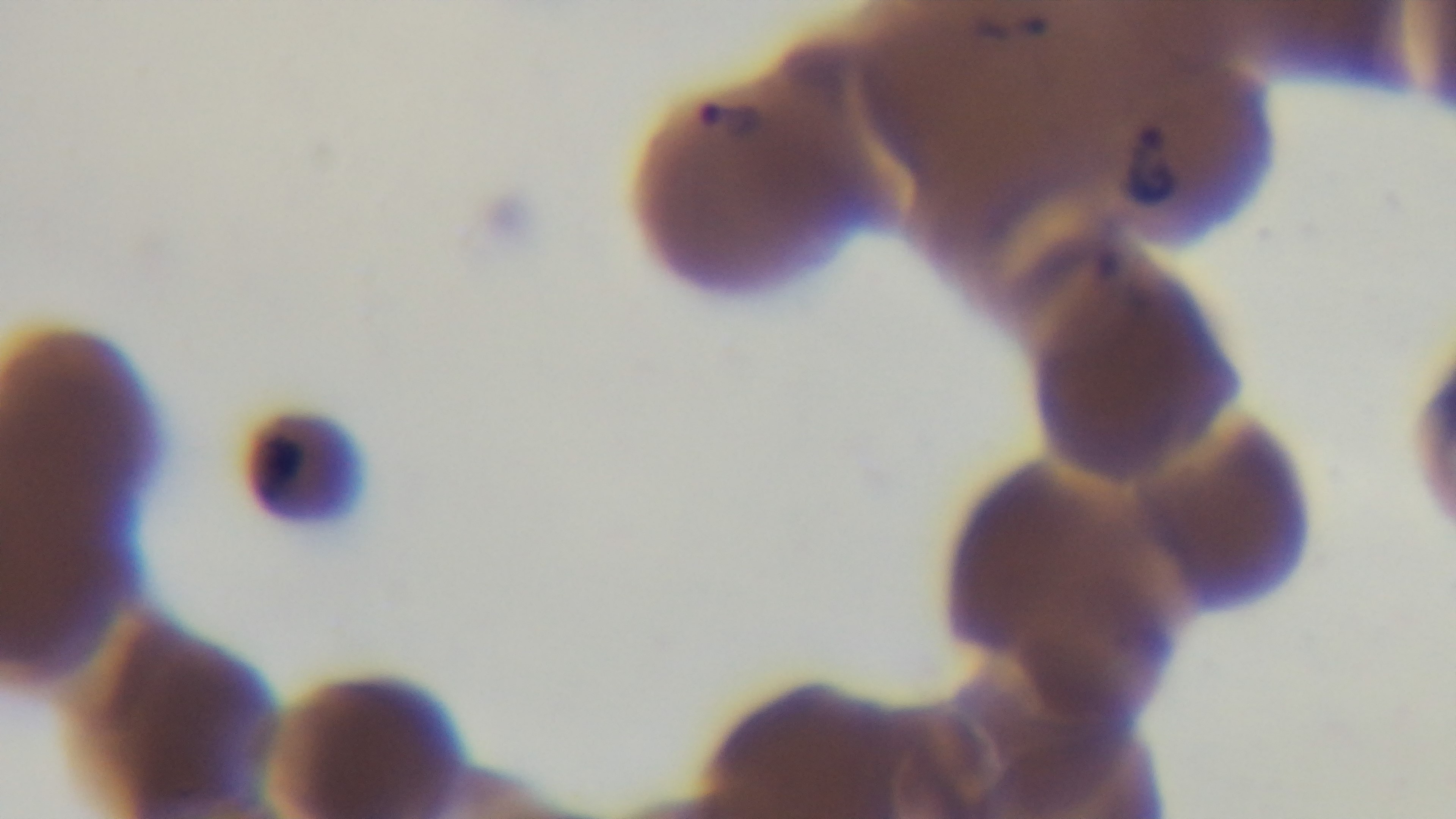
Summary:
  - Malaria status: infected
  - Preparation: thin
  - Stain: Giemsa
  - Modality: light microscopy
  - Capture: mounted 4K digital camera
  - Field of view: single
  - Objective: 100x oil immersion